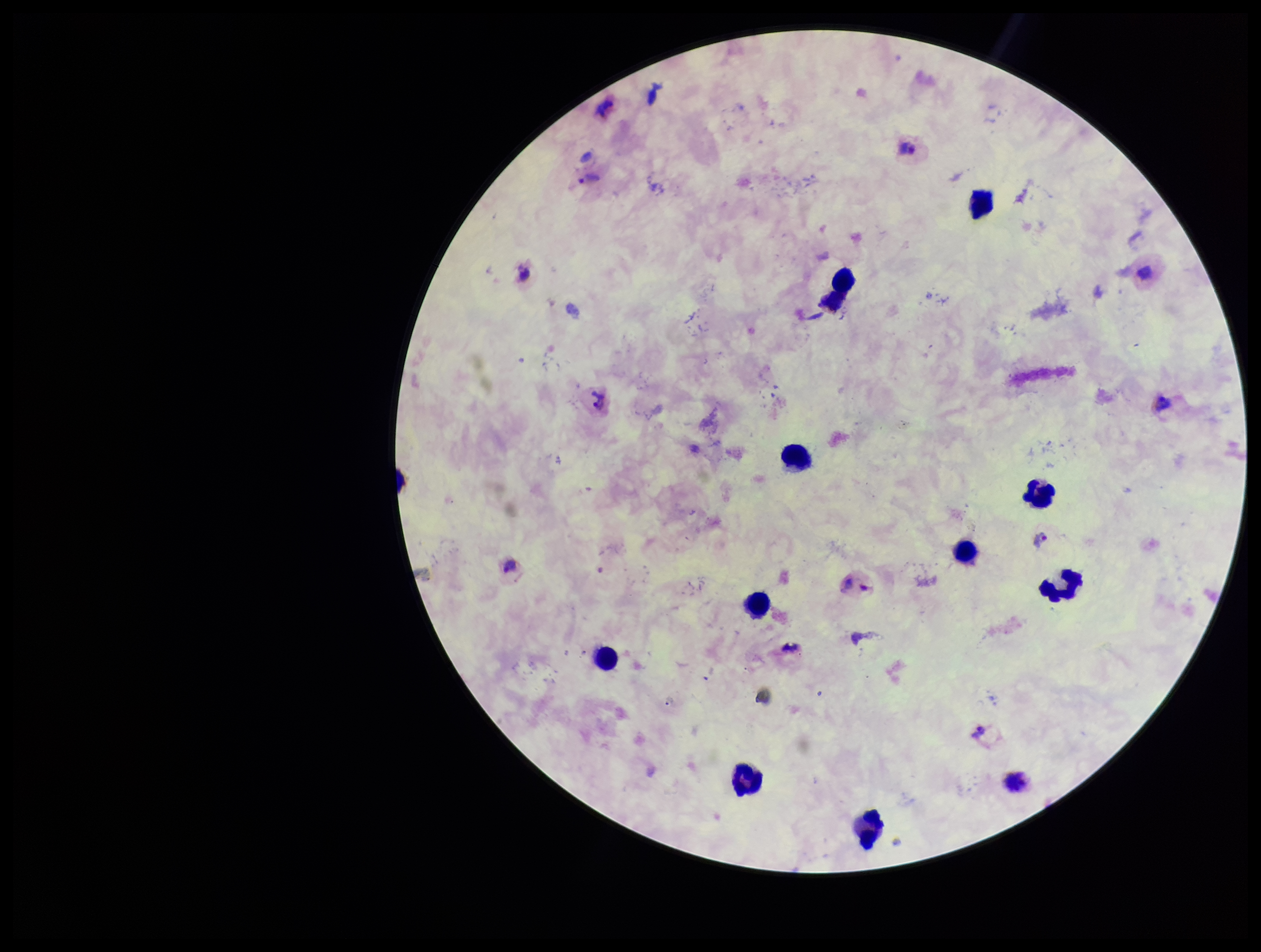
Summary:
  - Leukocyte count: 10
  - Image size: 1261×952 pixels
  - Patient malaria status: infected
  - Plasmodium parasites: seen
  - Parasite count: 4
  - Species reported for this patient: Plasmodium vivax
  - Preparation: thick smear
  - Capture: smartphone photograph through the microscope eyepiece
  - Stain: Giemsa
  - Field of view: single